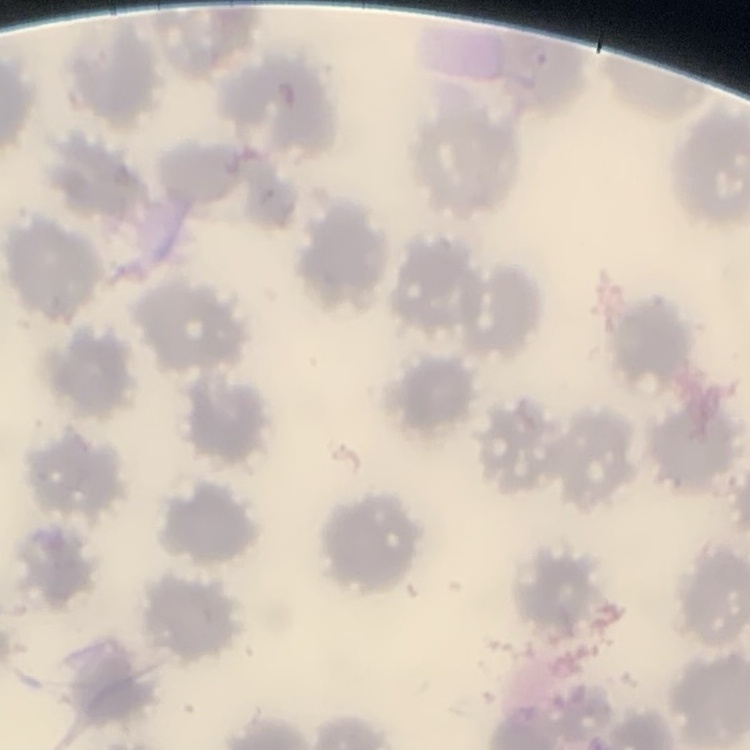
The erythrocytes exhibit no rouleaux formation. Thin peripheral smear. Square crop of a larger photomicrograph. Field's or Giemsa stain.